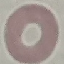
Malaria status: uninfected. Thin blood smear. Automatically extracted cell patch, resized to 64 × 64 pixels. Photographed with a smartphone camera at the microscope eyepiece. Giemsa-stained preparation.